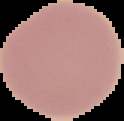
{
  "image_type": "segmented cell region with the area outside set to black",
  "image_size": "124×121 pixels",
  "result": "no Plasmodium parasites seen",
  "preparation": "thin blood smear"
}